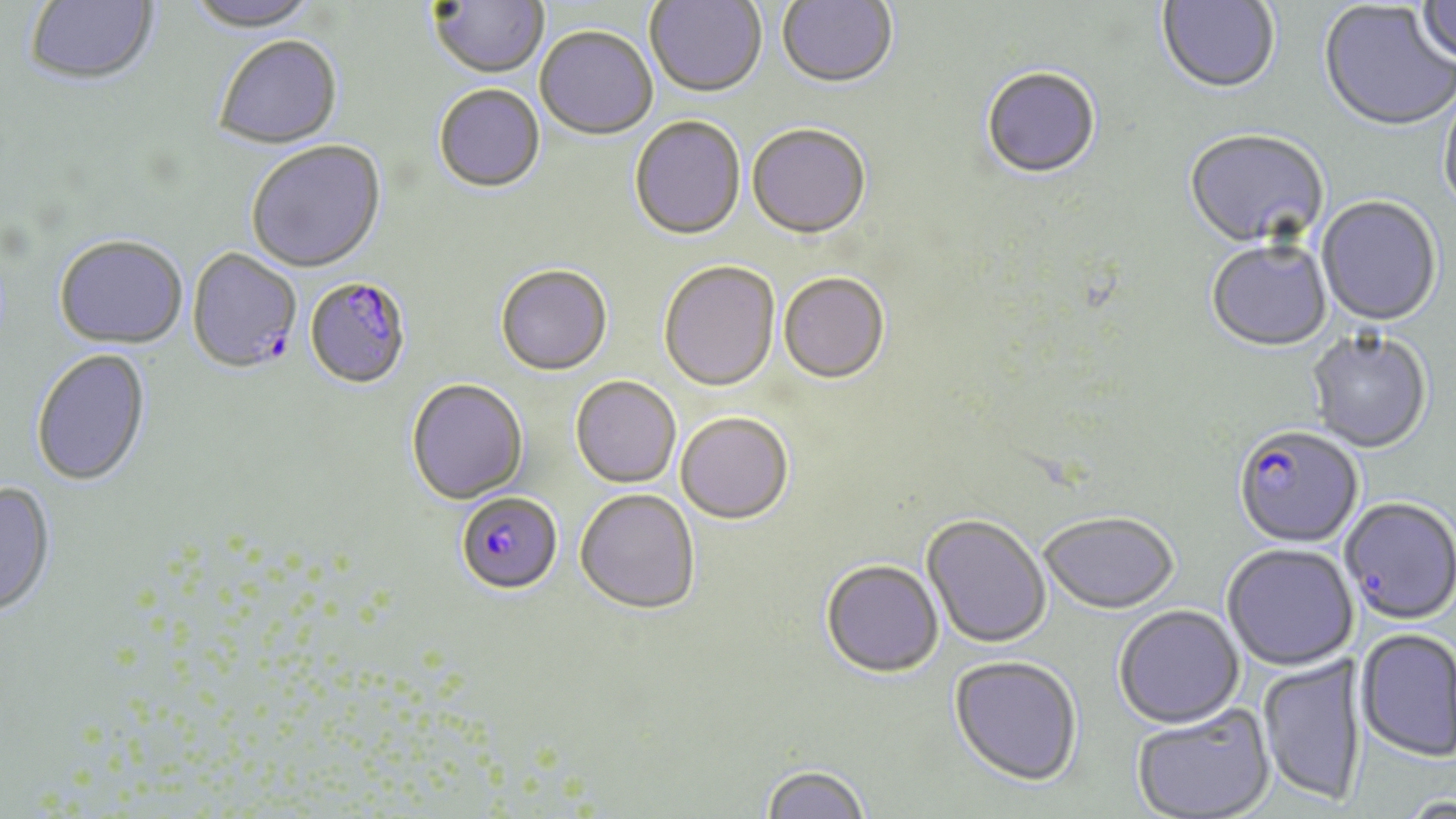
slide-level diagnosis = Plasmodium falciparum
uninfected red blood cell locations = approximate bounding boxes as [x1, y1, x2, y2] in pixels: [24, 0, 160, 89], [645, 0, 767, 99], [1157, 0, 1280, 96], [1414, 0, 1456, 67], [184, 1, 321, 35], [429, 1, 549, 81], [776, 1, 898, 91], [1318, 2, 1455, 135], [535, 27, 657, 141], [214, 37, 343, 151], [981, 68, 1101, 181], [433, 85, 545, 194], [1438, 91, 1456, 221], [629, 116, 746, 241], [746, 124, 871, 239], [1184, 130, 1328, 252], [246, 142, 386, 275], [1316, 198, 1442, 328], [54, 236, 188, 350], [1206, 241, 1332, 353], [658, 261, 780, 392], [495, 264, 612, 376], [778, 272, 889, 382], [1306, 330, 1432, 454], [31, 348, 152, 487], [570, 376, 681, 488], [406, 378, 528, 504], [676, 411, 793, 524], [0, 482, 56, 619], [575, 489, 700, 614], [1340, 497, 1455, 624], [1039, 511, 1179, 614], [921, 514, 1051, 649], [1222, 543, 1358, 670], [821, 559, 944, 678], [1114, 604, 1245, 728], [1355, 628, 1455, 762], [1256, 654, 1368, 808], [949, 655, 1083, 787], [1131, 705, 1275, 819], [759, 763, 870, 819], [1397, 796, 1455, 819]
modality = light microscopy
Plasmodium falciparum-infected red blood cell locations = approximate bounding boxes as [x1, y1, x2, y2] in pixels: [188, 249, 302, 372], [308, 275, 408, 387], [1233, 426, 1364, 549], [456, 492, 563, 594]
image size = 1456×819 pixels
stain = May-Grünwald-Giemsa
field of view = one of a larger specimen
magnification = 1000x
preparation = thin blood film